Classify this cell by malaria status.
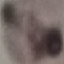

Uninfected.

image type = automatically extracted cell patch, resized to 64 × 64 pixels
preparation = thin blood smear
capture = smartphone camera at the microscope eyepiece
stain = Giemsa